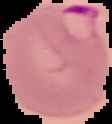
Summary:
  - Preparation: thin blood smear
  - Image type: segmented cell region on a black background
  - Image size: 112×124 pixels
  - Result: Plasmodium parasites detected